Identify the preparation type.
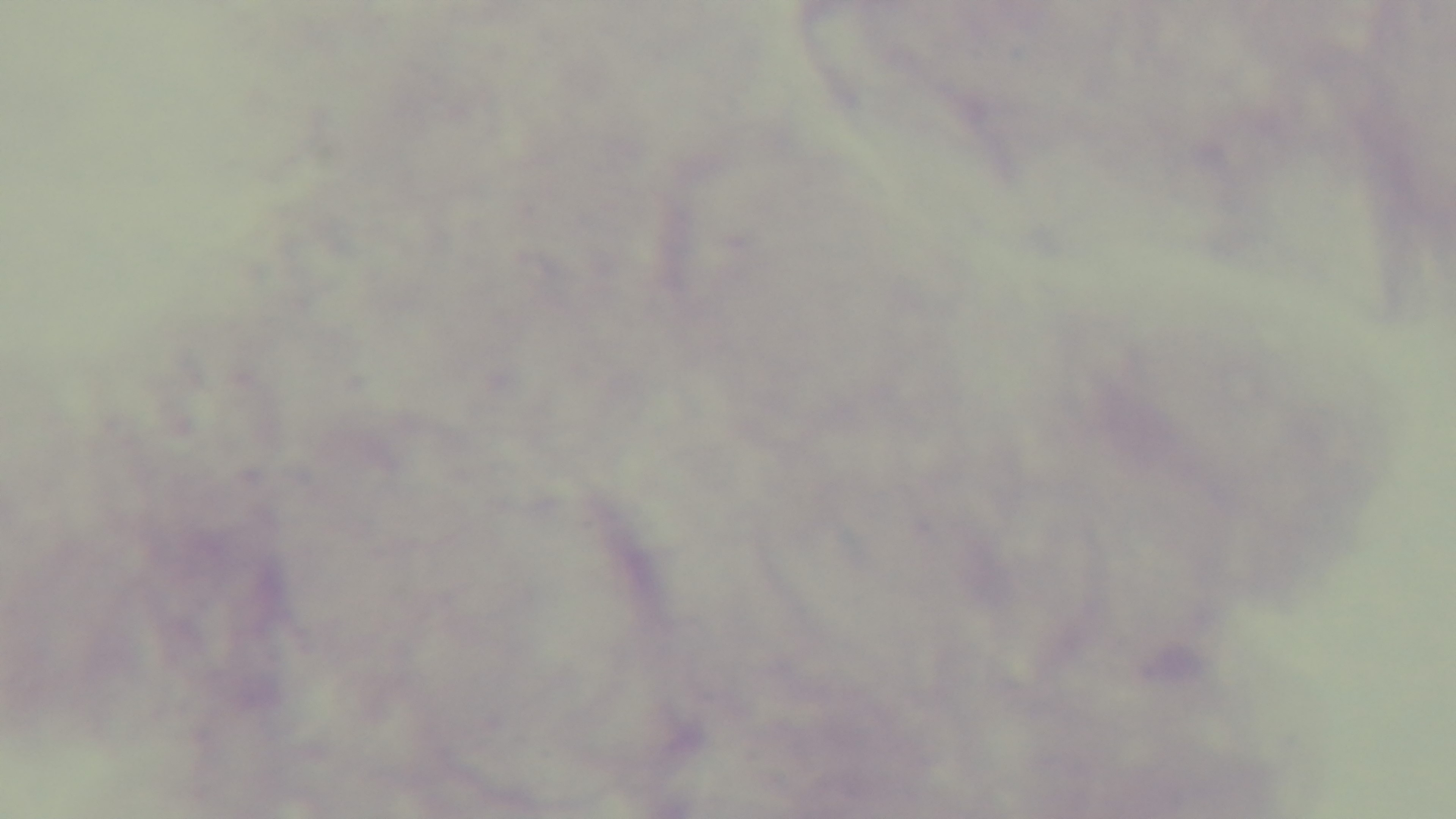

Thick.

Photomicrograph. One field from the slide. Giemsa-stained. Malaria status: uninfected. Mounted 4K digital camera. 100x oil-immersion objective.